Evaluate for malaria.
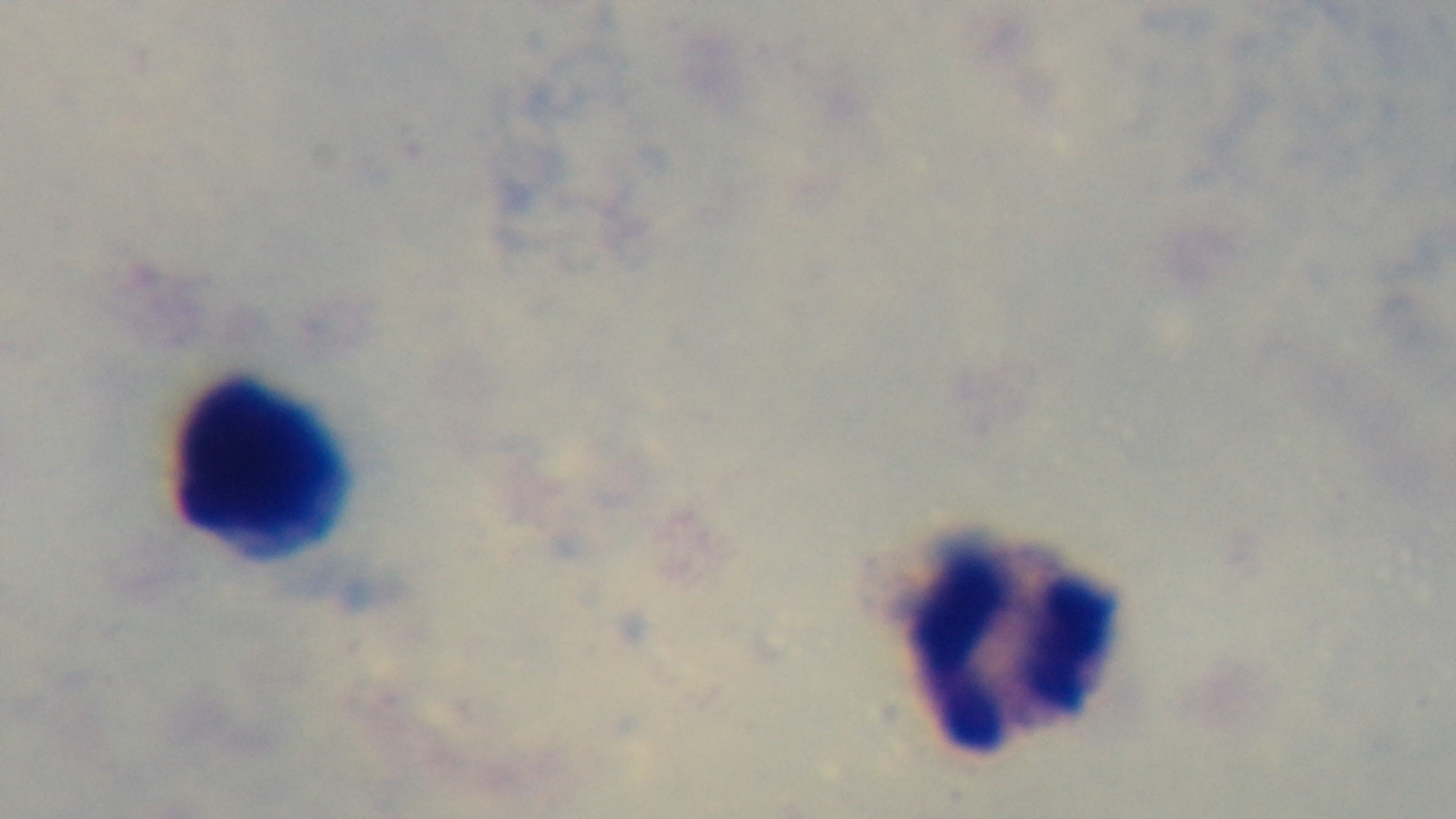

It is uninfected.

Summary:
  - Modality: light microscopy
  - Field of view: single
  - Preparation: thick
  - Capture: mounted 4K digital camera
  - Objective: 100x oil immersion
  - Stain: Giemsa